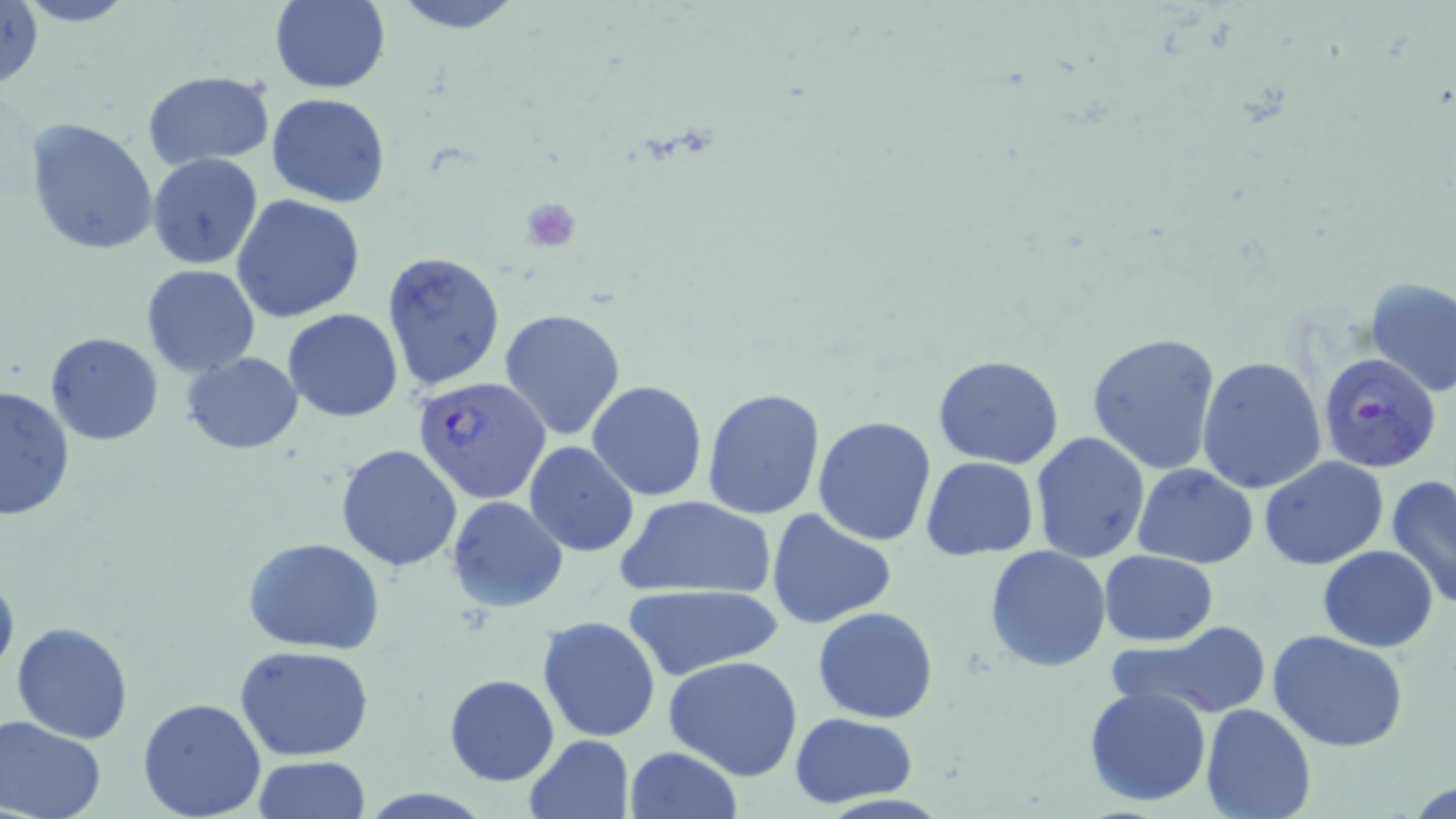

Approximate bounding boxes as named x1/y1/x2/y2 corners in pixels. Uninfected red blood cell locations: (x1=1, y1=0, x2=45, y2=92), (x1=11, y1=0, x2=141, y2=28), (x1=268, y1=0, x2=390, y2=93), (x1=392, y1=0, x2=525, y2=34), (x1=142, y1=71, x2=274, y2=167), (x1=266, y1=93, x2=393, y2=207), (x1=27, y1=116, x2=161, y2=256), (x1=147, y1=154, x2=265, y2=271), (x1=144, y1=165, x2=353, y2=292), (x1=232, y1=194, x2=366, y2=322), (x1=381, y1=251, x2=507, y2=395), (x1=141, y1=264, x2=261, y2=378), (x1=1363, y1=277, x2=1456, y2=400), (x1=500, y1=308, x2=626, y2=441), (x1=284, y1=309, x2=402, y2=422), (x1=1086, y1=331, x2=1222, y2=475), (x1=44, y1=332, x2=164, y2=445), (x1=181, y1=351, x2=302, y2=454), (x1=934, y1=355, x2=1064, y2=468), (x1=1197, y1=356, x2=1327, y2=494), (x1=587, y1=379, x2=708, y2=501), (x1=0, y1=383, x2=77, y2=523), (x1=701, y1=387, x2=825, y2=522), (x1=812, y1=415, x2=937, y2=547), (x1=1030, y1=433, x2=1150, y2=563), (x1=524, y1=440, x2=640, y2=558), (x1=335, y1=444, x2=464, y2=573), (x1=921, y1=456, x2=1038, y2=560), (x1=1258, y1=456, x2=1389, y2=570), (x1=1132, y1=464, x2=1258, y2=567), (x1=1385, y1=474, x2=1456, y2=610), (x1=445, y1=495, x2=569, y2=613), (x1=616, y1=495, x2=777, y2=600), (x1=766, y1=508, x2=897, y2=629), (x1=242, y1=538, x2=386, y2=654), (x1=985, y1=544, x2=1111, y2=671), (x1=1317, y1=546, x2=1439, y2=651), (x1=1099, y1=550, x2=1218, y2=646), (x1=0, y1=564, x2=20, y2=687), (x1=623, y1=583, x2=783, y2=681), (x1=813, y1=606, x2=939, y2=723), (x1=537, y1=615, x2=661, y2=742), (x1=10, y1=622, x2=134, y2=743), (x1=1113, y1=624, x2=1269, y2=719), (x1=1269, y1=630, x2=1409, y2=752), (x1=234, y1=644, x2=375, y2=761), (x1=664, y1=655, x2=805, y2=781), (x1=443, y1=673, x2=558, y2=786), (x1=1085, y1=685, x2=1213, y2=807), (x1=137, y1=697, x2=268, y2=819), (x1=1201, y1=704, x2=1318, y2=819), (x1=789, y1=712, x2=918, y2=807), (x1=1, y1=715, x2=105, y2=819), (x1=523, y1=734, x2=634, y2=819), (x1=622, y1=746, x2=743, y2=819), (x1=253, y1=755, x2=370, y2=819). Plasmodium falciparum-infected red blood cell locations: (x1=1318, y1=353, x2=1444, y2=473), (x1=412, y1=374, x2=551, y2=503). Platelet locations: (x1=522, y1=198, x2=579, y2=252). Slide-level diagnosis: Plasmodium falciparum. 1000x magnification. Image is 1456×819 pixels. May-Grünwald-Giemsa-stained preparation. Light microscopy. One field of a larger specimen. Thin blood smear.